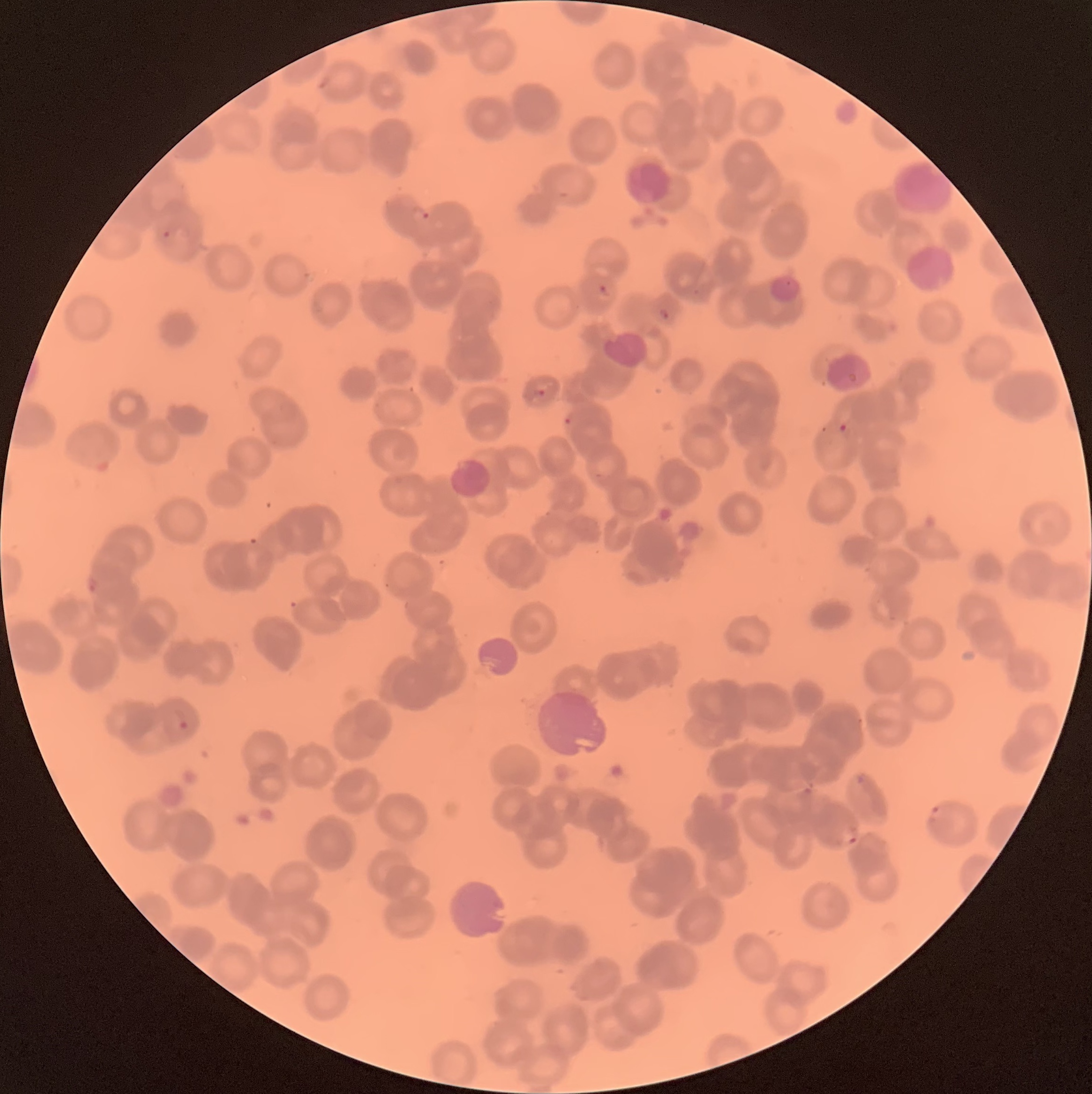
preparation: thin blood film
plasmodium_parasites_too_small_for_a_box: 'approximate object centers, named x/y in pixels: (x=696, y=291)'
red_blood_cell_morphology: rouleaux formation
image_size: 1092×1094 pixels
plasmodium_parasite_locations: 'approximate bounding boxes as named x1/y1/x2/y2 corners in pixels: (x1=422, y1=211, x2=430, y2=220), (x1=162, y1=230, x2=171, y2=239), (x1=598, y1=284, x2=610, y2=294), (x1=658, y1=308, x2=670, y2=320), (x1=536, y1=389, x2=546, y2=397), (x1=564, y1=416, x2=573, y2=427), (x1=838, y1=424, x2=847, y2=433), (x1=86, y1=577, x2=100, y2=593), (x1=173, y1=707, x2=189, y2=729), (x1=931, y1=804, x2=942, y2=819), (x1=841, y1=830, x2=859, y2=845)'
modality: light microscopy